Locate malaria parasites and identify their life-cycle stages.
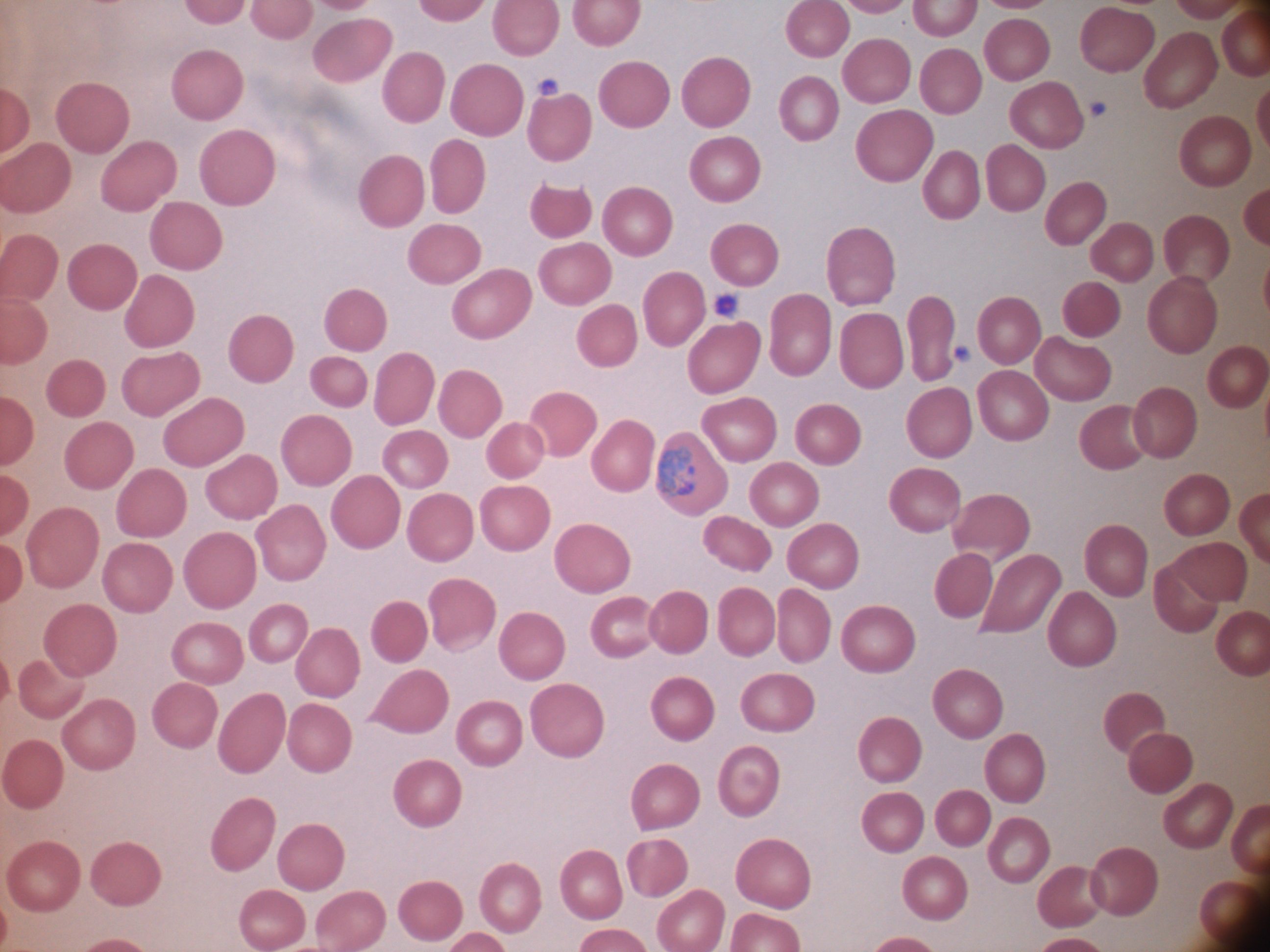

Approximate bounding boxes as (x1,y1)-(x2,y2) corner pairs in pixels, from the source annotation, which is not necessarily exhaustive.
Trophozoites: (656,446)-(696,499).

magnification: 100x
species: Plasmodium ovale
stain: Giemsa
field_of_view: one from this slide
preparation: thin blood film
microscope: Leica DM2000 with built-in camera
image_size: 1270×952 pixels